Report the malaria status of this cell.
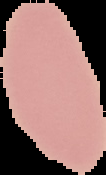

It is uninfected.

{
  "image_type": "segmented cell region with the area outside set to black",
  "preparation": "thin blood smear",
  "image_size": "106×175 pixels"
}